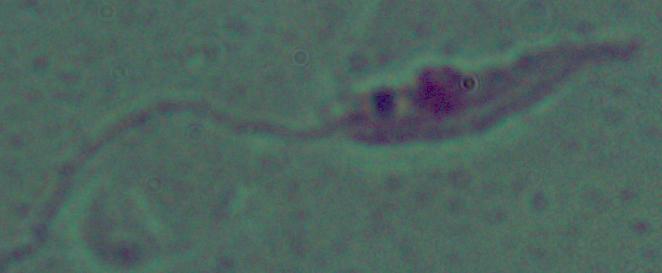
Summary:
  - Identification: Leishmania
  - Magnification: 1000x
  - Modality: micrograph